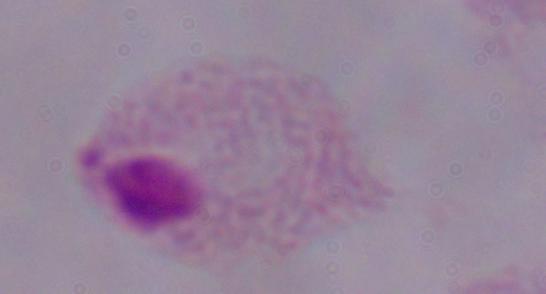 Photomicrograph. 1000x magnification. A trichomonad is shown.